Name the blood parasite species.
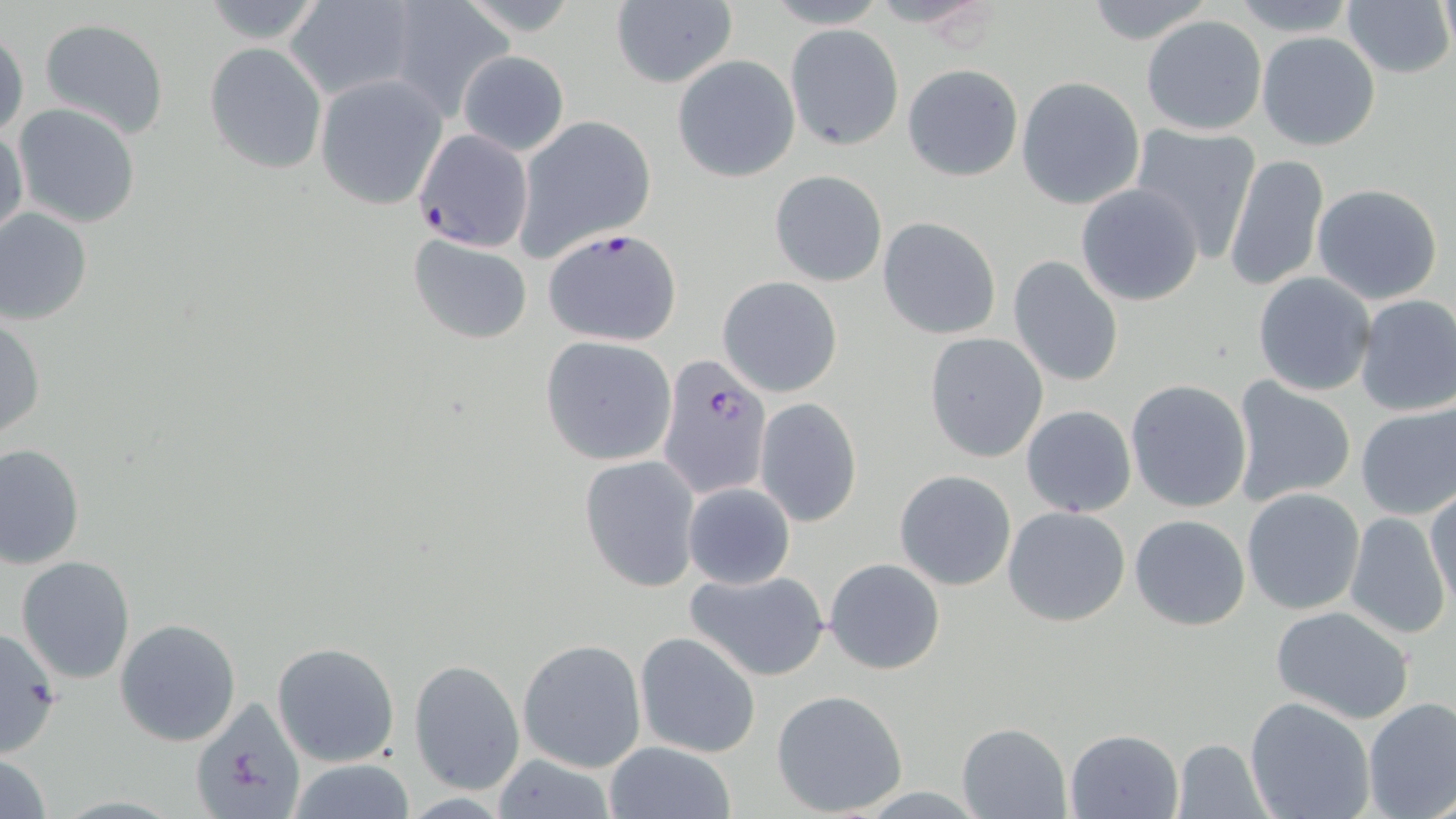
Plasmodium falciparum.

stain: May-Grünwald-Giemsa
plasmodium_falciparum_infected_red_blood_cell_locations: 'approximate bounding boxes as (x1,y1)-(x2,y2) corner pairs in pixels: (411,128)-(535,252), (543,228)-(684,347), (658,356)-(771,501)'
modality: light microscopy
field_of_view: one of a larger specimen
uninfected_red_blood_cell_locations: 'approximate bounding boxes as (x1,y1)-(x2,y2) corner pairs in pixels: (867,0)-(1006,32), (1079,0)-(1219,45), (1222,0)-(1362,35), (1437,0)-(1455,62), (196,1)-(331,48), (285,1)-(421,101), (386,1)-(510,116), (610,2)-(738,89), (1343,2)-(1454,80), (1139,14)-(1268,137), (37,17)-(171,139), (785,23)-(902,151), (0,28)-(27,143), (1256,32)-(1380,152), (204,42)-(327,174), (458,50)-(569,155), (672,55)-(800,182), (902,62)-(1023,181), (315,74)-(448,211), (1016,77)-(1145,210), (13,103)-(142,228), (514,115)-(657,257), (1127,121)-(1263,261), (1,123)-(27,239), (1222,154)-(1328,292), (770,169)-(888,286), (1075,183)-(1204,305), (1312,183)-(1443,303), (0,208)-(94,325), (878,218)-(1002,339), (407,235)-(534,344), (1007,256)-(1124,389), (1251,271)-(1377,397), (718,276)-(842,397), (1353,294)-(1456,417), (1,314)-(46,441), (923,332)-(1050,462), (539,336)-(676,466), (1124,378)-(1253,514), (1229,378)-(1357,507), (754,398)-(862,526), (1355,403)-(1456,520), (1021,406)-(1137,517), (1,443)-(85,569), (581,455)-(702,592), (894,469)-(1017,591), (682,482)-(795,589), (1242,487)-(1365,614), (1426,489)-(1456,616), (1001,505)-(1132,627), (1345,513)-(1450,640), (1129,515)-(1251,630), (15,555)-(137,684), (824,557)-(945,675), (680,567)-(832,682), (1270,603)-(1416,723), (114,617)-(241,747), (0,628)-(63,755), (634,630)-(762,758), (517,637)-(647,773), (271,641)-(400,767), (408,658)-(525,794), (771,690)-(908,817), (188,696)-(308,818), (1244,696)-(1375,819), (1361,697)-(1456,819), (956,721)-(1073,818), (1065,729)-(1183,819), (1171,737)-(1270,817), (604,742)-(736,819), (0,750)-(52,819), (489,754)-(620,818), (282,759)-(421,817)'
preparation: thin blood film
magnification: 1000x
image_size: 1456×819 pixels